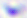

modality = photomicrograph
magnification = 400x
identification = Toxoplasma gondii